Point out each leukocyte.
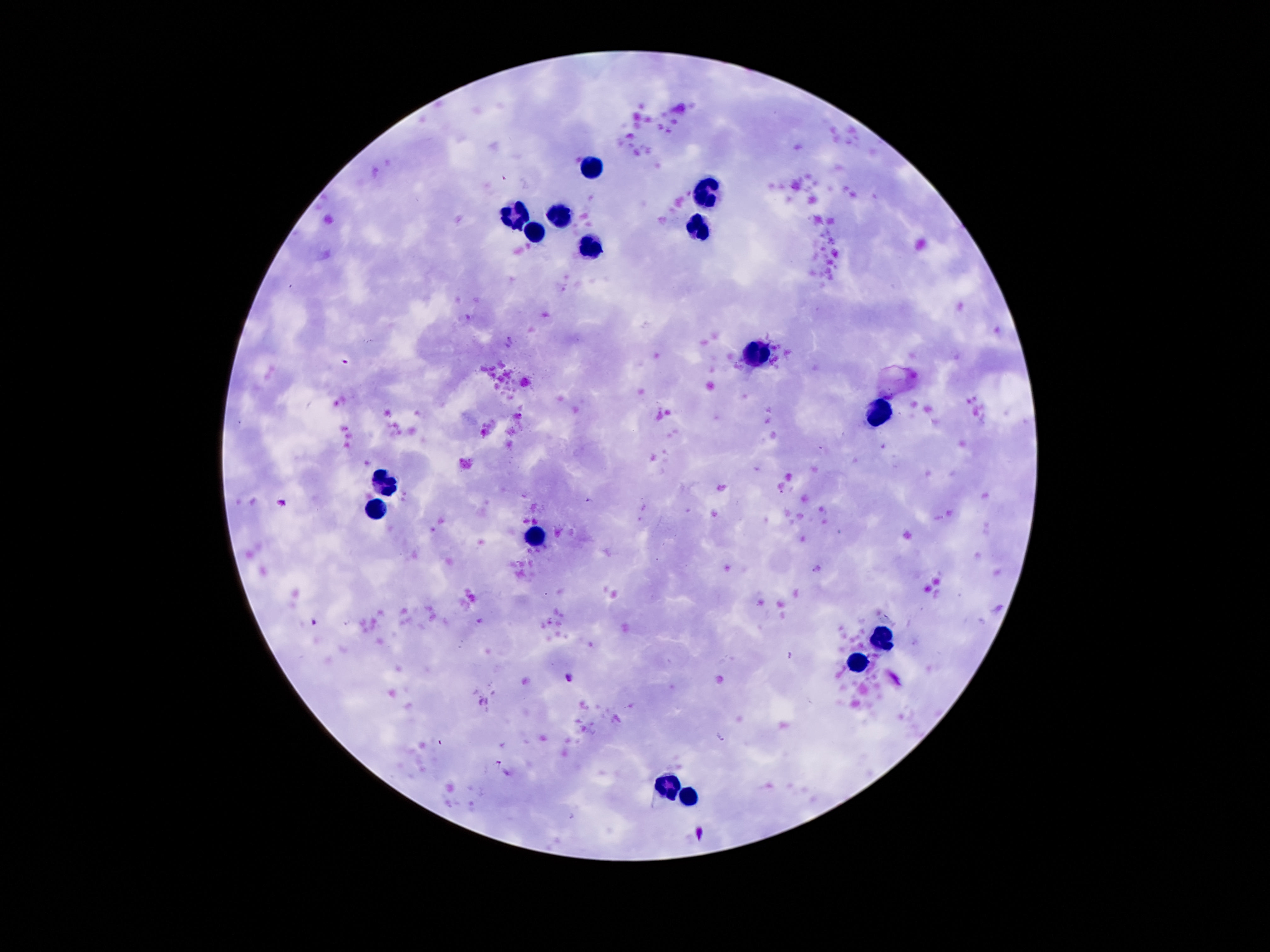

Approximate object centers, in pixels from the top-left corner.
Leukocytes: (x=592, y=168), (x=705, y=193), (x=559, y=217), (x=516, y=219), (x=698, y=227), (x=535, y=234), (x=588, y=246), (x=754, y=354), (x=879, y=414), (x=385, y=484), (x=375, y=506), (x=539, y=537), (x=881, y=639), (x=856, y=658), (x=670, y=783), (x=688, y=793).

Summary:
  - Image size: 1270×952 pixels
  - Capture: smartphone camera through the microscope eyepiece
  - Stain: Giemsa
  - Patient malaria status: not infected
  - Magnification: 100x
  - Field of view: one from this slide
  - Preparation: thick blood film